Point out each malaria parasite.
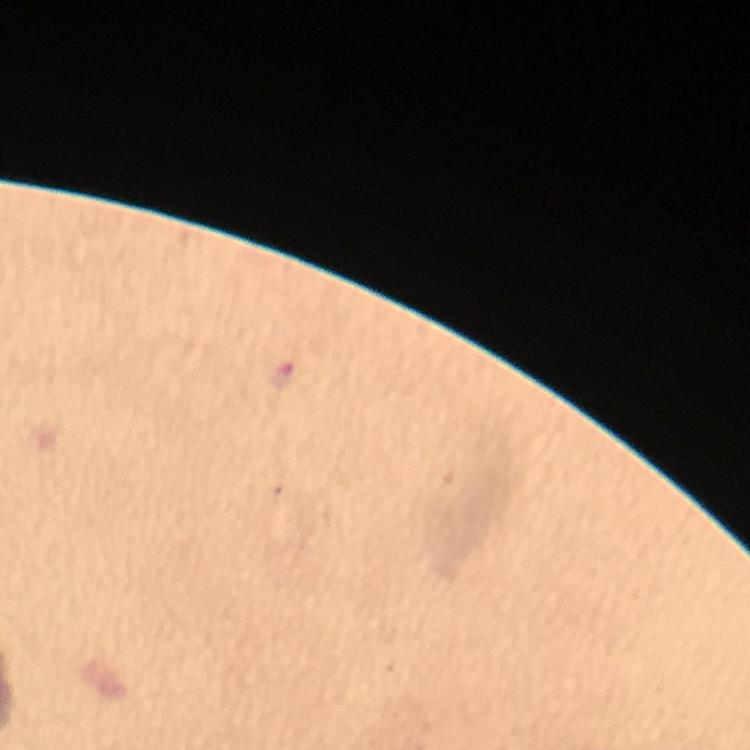

Approximate centers as {x, y} in pixels.
Malaria parasites: {283, 376}.

Summary:
  - Preparation: thick blood film
  - Image size: 750×750 pixels
  - Context: from a diagnostic examination for malaria
  - Stain: Giemsa
  - Cropped from: a single field of view
  - Immersion oil: applied
  - Capture: smartphone mounted on the microscope
  - Magnification: 100x